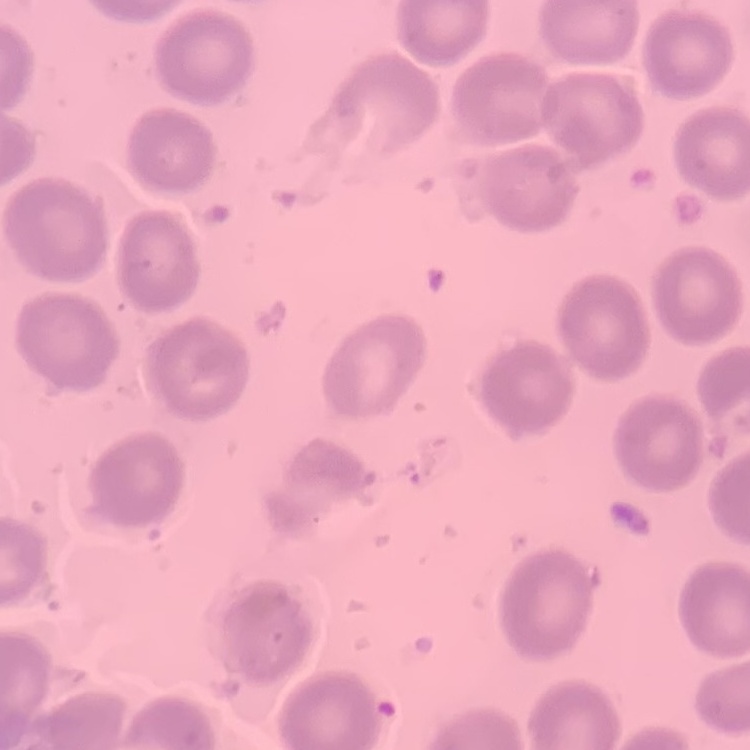
Summary:
  - Red blood cell morphology: no rouleaux formation
  - Stain: Field's or Giemsa
  - Image type: square crop of a larger photomicrograph
  - Preparation: thin blood smear